Classify this cell by malaria status.
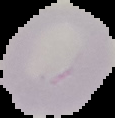
Uninfected.

Image is 115×118 pixels. Segmented cell region on a black background. From a thin blood smear.